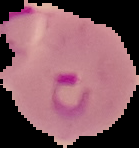
From a thin blood film. Malaria status: parasitized. Image is 139×148 pixels. Segmented cell region on a black background.